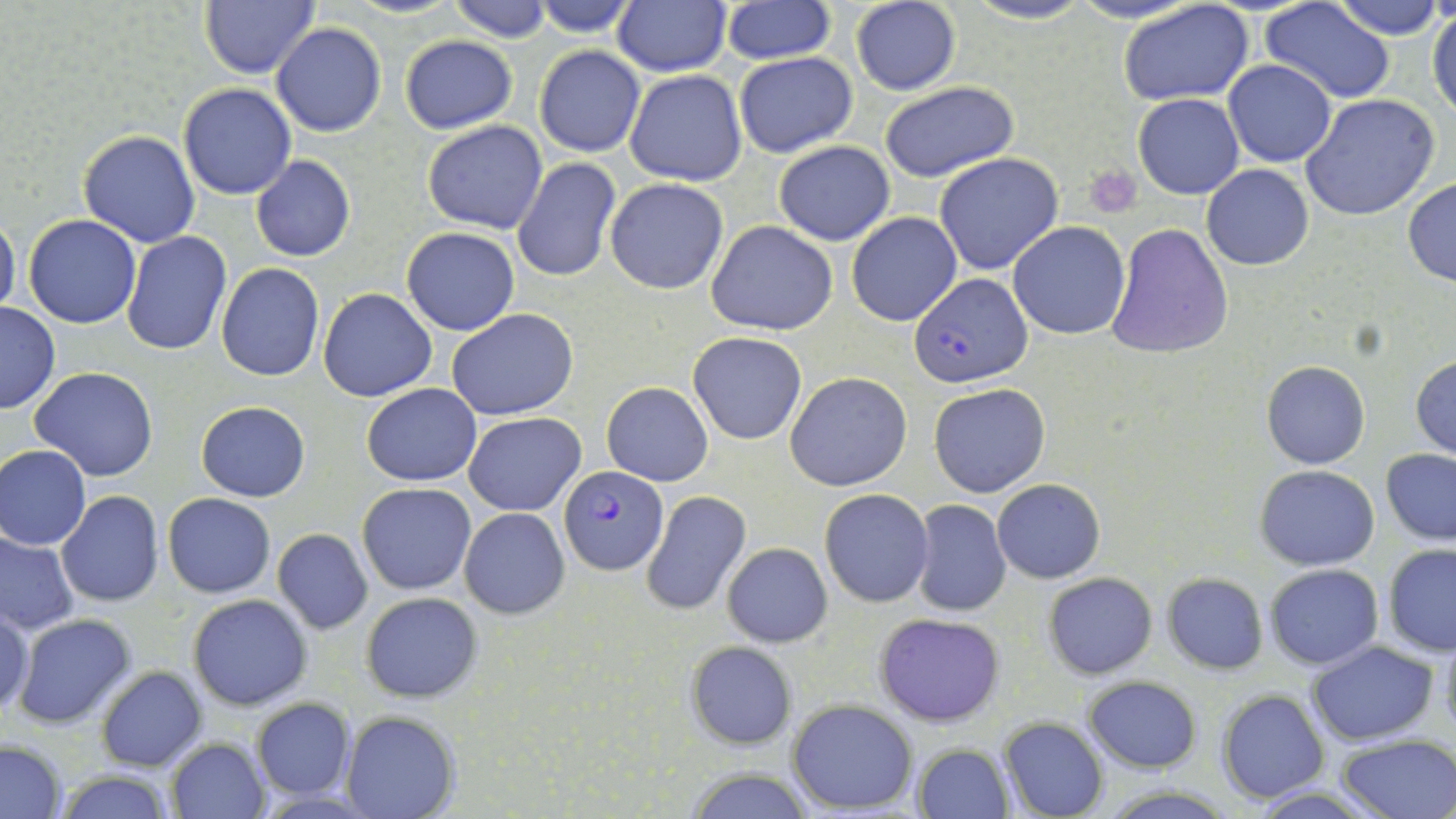
Summary:
  - Coordinate format: approximate bounding boxes as (x1,y1)-(x2,y2) corner pairs in pixels
  - Uninfected red blood cell locations: (199,0)-(321,79), (446,0)-(554,42), (612,0)-(730,75), (961,0)-(1096,27), (1334,0)-(1444,39), (531,1)-(639,37), (1118,1)-(1256,105), (721,2)-(835,64), (851,2)-(961,95), (1262,2)-(1395,102), (1428,6)-(1456,118), (270,22)-(387,138), (399,35)-(517,133), (534,46)-(645,158), (734,52)-(859,158), (579,53)-(707,173), (1223,59)-(1338,167), (625,68)-(748,186), (878,80)-(1019,183), (178,83)-(298,200), (1133,93)-(1244,199), (1300,94)-(1440,221), (421,121)-(548,234), (78,129)-(200,247), (774,142)-(893,245), (934,153)-(1064,276), (251,156)-(356,261), (512,158)-(620,283), (1202,164)-(1315,270), (604,177)-(727,294), (1402,178)-(1456,286), (0,211)-(20,319), (846,211)-(964,327), (23,214)-(141,328), (705,221)-(839,334), (1007,222)-(1130,338), (1106,222)-(1233,359), (402,227)-(520,335), (122,231)-(231,356), (216,263)-(325,381), (318,288)-(436,401), (1,302)-(60,414), (447,309)-(579,421), (688,331)-(807,445), (1411,354)-(1456,459), (1261,359)-(1370,469), (29,367)-(159,482), (786,371)-(912,491), (603,382)-(713,485), (928,382)-(1050,497), (362,384)-(482,486), (186,397)-(296,594), (196,400)-(310,501), (465,412)-(586,515), (0,445)-(91,550), (1381,448)-(1456,546), (1256,465)-(1380,569), (991,478)-(1105,583), (358,482)-(477,596), (820,489)-(934,608), (642,491)-(750,616), (56,492)-(165,608), (163,493)-(275,597), (911,499)-(1012,615), (459,507)-(570,619), (272,529)-(372,634), (0,531)-(79,634), (723,542)-(831,647), (1382,544)-(1456,655), (1263,563)-(1383,670), (1044,572)-(1157,679), (1162,573)-(1268,674), (362,591)-(483,703), (188,593)-(313,710), (1,606)-(34,718), (875,611)-(1004,727), (11,612)-(137,729), (1439,623)-(1456,743), (685,640)-(796,749), (1308,641)-(1439,745), (96,665)-(206,771), (1082,676)-(1202,772), (1216,689)-(1329,804), (251,697)-(355,800), (789,700)-(919,815), (342,712)-(458,819), (999,717)-(1108,819), (1337,733)-(1456,817), (166,737)-(269,818), (0,740)-(66,817), (913,744)-(1014,818), (681,766)-(815,819), (53,768)-(179,819), (1099,783)-(1237,817)
  - Plasmodium falciparum-infected red blood cell locations: (912,273)-(1032,386), (559,467)-(668,576)
  - Platelet locations: (1082,164)-(1142,218)
  - Slide-level diagnosis: Plasmodium falciparum
  - Magnification: 1000x
  - Image size: 1456×819 pixels
  - Field of view: single
  - Preparation: thin blood smear
  - Stain: May-Grünwald-Giemsa
  - Modality: optical microscopy